Identify the preparation type.
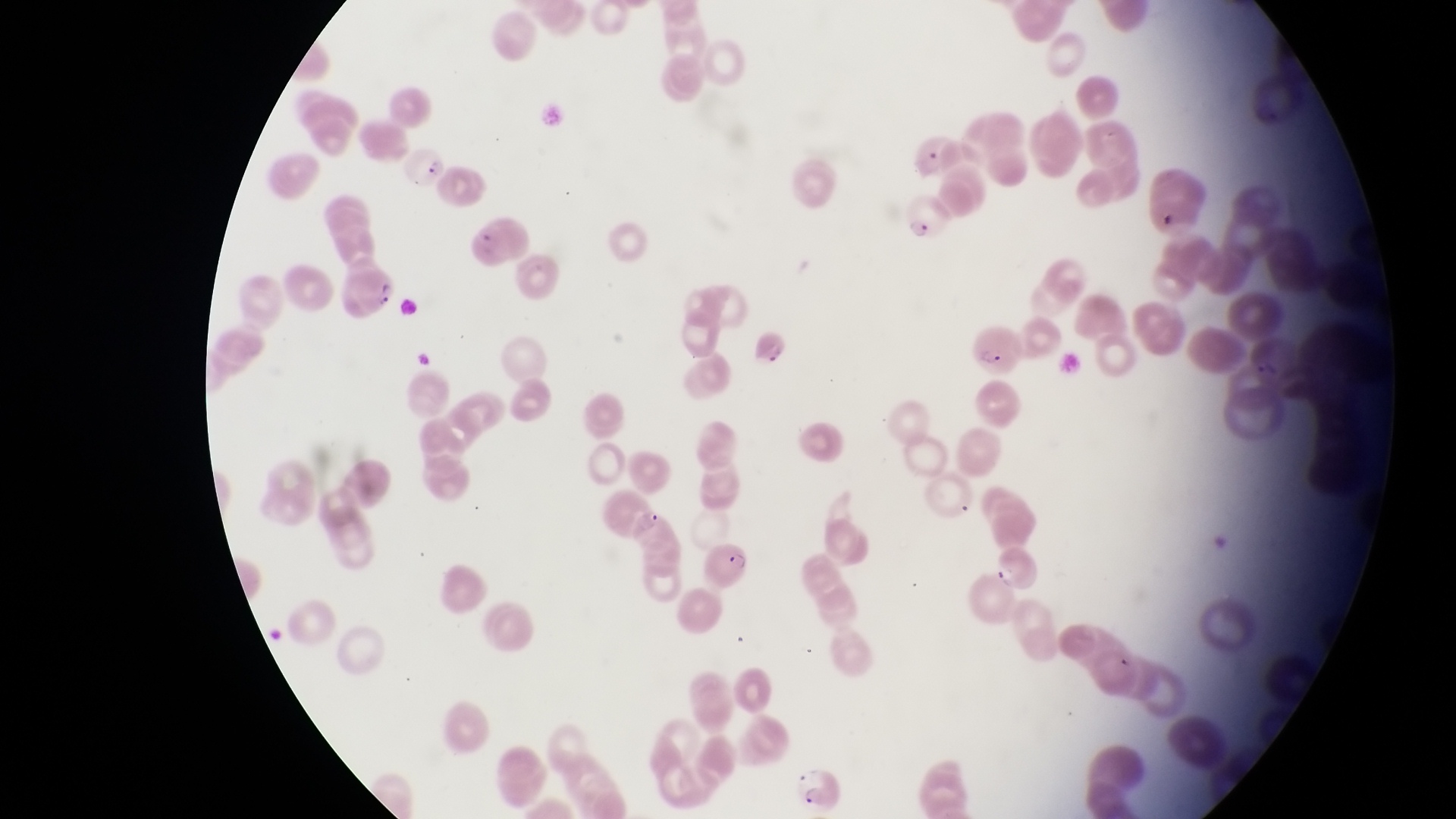

Thin blood smear.

Approximate bounding boxes as [left, top, right, bottom] in pixels. Parasitised red blood cell locations: [399, 148, 452, 187], [904, 192, 953, 241], [460, 211, 531, 271], [346, 258, 401, 321], [967, 322, 1028, 380], [697, 541, 749, 596], [988, 548, 1044, 591], [793, 759, 845, 809]. One field of view. Sample from Uganda. Magnification of 1000x. Photographed through the eyepiece of an Olympus CX-23 microscope with a smartphone camera. Image is 1456×819 pixels.